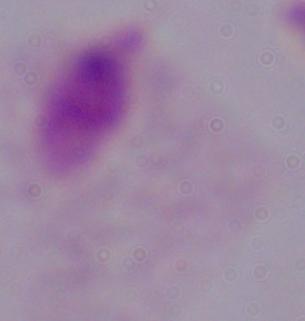
magnification = 1000x
identification = trichomonad
modality = micrograph